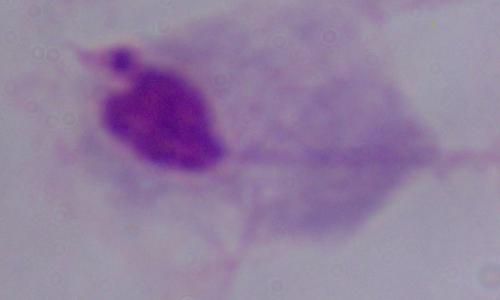

modality: micrograph
magnification: 1000x
identification: trichomonad